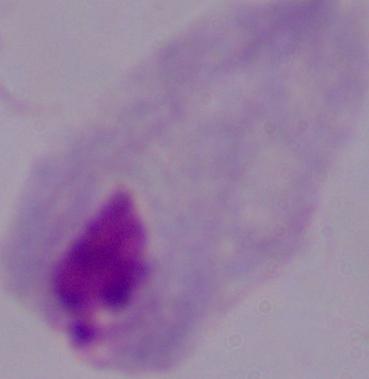

magnification = 1000x
identification = trichomonad
modality = micrograph